Assess this cell for malaria.
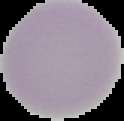

Uninfected.

Image is 124×121 pixels. Segmented cell region on a black background. From a thin blood film.